Assess the morphology of the red blood cells.
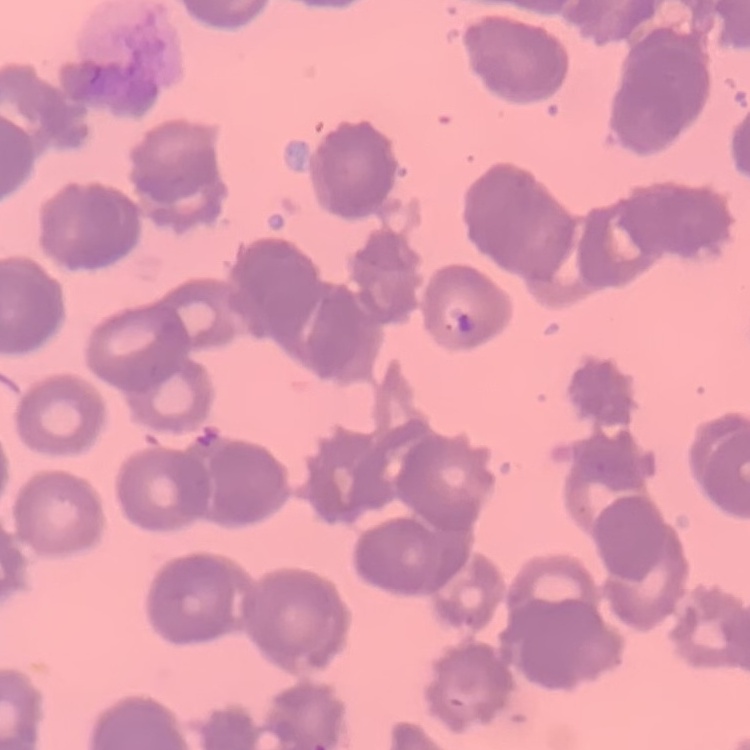
They show rouleaux formation.

Summary:
  - Preparation: thin blood smear
  - Image type: one tile cut from a larger photomicrograph
  - Stain: Field's or Giemsa